Report the malaria status of this cell.
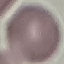

It is uninfected.

Summary:
  - Preparation: thin blood film
  - Capture: smartphone through the microscope eyepiece
  - Stain: Giemsa
  - Image type: automatically extracted cell patch, resized to 64 × 64 pixels